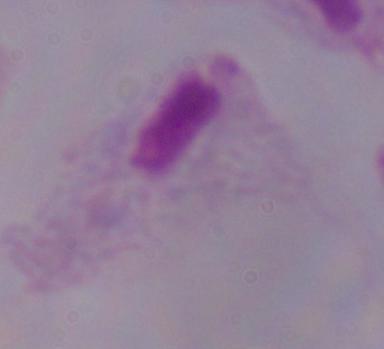
Summary:
  - Identification: trichomonad
  - Magnification: 1000x
  - Modality: micrograph